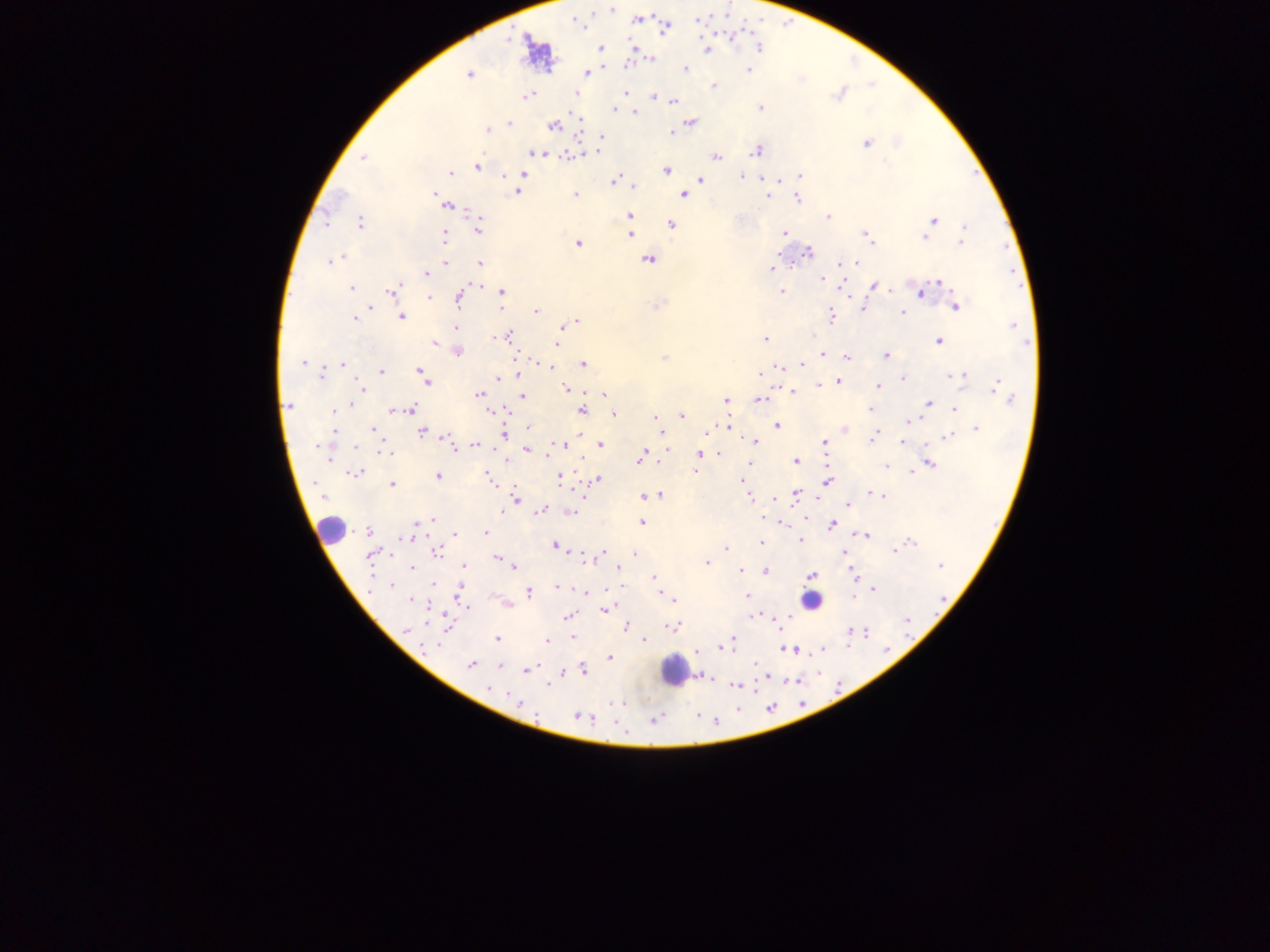

Approximate centers as {x, y} in pixels.
Summary:
  - Leukocyte locations: {330, 529}, {810, 601}, {674, 670}
  - Plasmodium parasite locations: {612, 8}, {697, 19}, {576, 20}, {637, 20}, {665, 29}, {530, 45}, {759, 47}, {601, 48}, {706, 49}, {651, 59}, {686, 70}, {748, 70}, {587, 73}, {469, 74}, {714, 86}, {625, 92}, {575, 93}, {838, 94}, {527, 95}, {654, 96}, {673, 100}, {760, 108}, {614, 110}, {635, 112}, {690, 122}, {509, 123}, {553, 126}, {487, 130}, {670, 132}, {602, 137}, {866, 144}, {598, 149}, {757, 150}, {535, 153}, {567, 156}, {715, 156}, {363, 158}, {477, 167}, {666, 171}, {451, 173}, {523, 174}, {800, 175}, {741, 176}, {701, 180}, {614, 181}, {635, 186}, {517, 191}, {434, 193}, {574, 194}, {683, 196}, {767, 196}, {798, 198}, {448, 207}, {630, 215}, {828, 216}, {934, 220}, {326, 221}, {360, 223}, {672, 225}, {964, 226}, {479, 227}, {784, 233}, {631, 234}, {444, 235}, {867, 237}, {925, 237}, {870, 240}, {962, 240}, {577, 244}, {808, 252}, {340, 259}, {649, 259}, {331, 261}, {445, 262}, {479, 262}, {854, 263}, {772, 269}, {425, 274}, {822, 279}, {941, 282}, {478, 285}, {875, 286}, {351, 288}, {391, 291}, {781, 291}, {501, 292}, {922, 292}, {429, 298}, {459, 299}, {658, 306}, {956, 306}, {863, 307}, {369, 308}, {535, 311}, {903, 312}, {402, 316}, {831, 316}, {355, 317}, {576, 322}, {568, 324}, {1013, 326}, {456, 328}, {561, 328}, {498, 337}, {507, 337}, {764, 339}, {938, 342}, {434, 343}, {557, 344}, {458, 352}, {822, 354}, {885, 355}, {665, 358}, {847, 358}, {302, 363}, {343, 364}, {583, 364}, {802, 365}, {549, 366}, {780, 366}, {420, 370}, {321, 371}, {381, 372}, {519, 373}, {761, 373}, {960, 376}, {498, 379}, {903, 379}, {425, 380}, {838, 382}, {819, 384}, {878, 386}, {997, 386}, {363, 388}, {565, 388}, {793, 391}, {478, 394}, {604, 394}, {523, 397}, {760, 399}, {1010, 399}, {726, 400}, {929, 404}, {290, 405}, {350, 405}, {410, 408}, {869, 409}, {955, 409}, {335, 410}, {393, 410}, {490, 411}, {582, 411}, {614, 414}, {682, 415}, {657, 418}, {911, 420}, {726, 425}, {777, 426}, {529, 427}, {374, 429}, {845, 429}, {976, 429}, {334, 431}, {422, 433}, {504, 435}, {663, 436}, {873, 437}, {947, 437}, {754, 441}, {824, 442}, {903, 442}, {601, 444}, {451, 445}, {476, 445}, {562, 445}, {355, 446}, {321, 448}, {528, 449}, {667, 450}, {386, 452}, {719, 454}, {699, 455}, {642, 457}, {327, 458}, {795, 461}, {930, 464}, {887, 466}, {912, 472}, {355, 473}, {438, 477}, {489, 477}, {560, 479}, {597, 480}, {743, 481}, {827, 482}, {392, 484}, {796, 493}, {875, 494}, {660, 495}, {644, 496}, {879, 496}, {322, 497}, {749, 498}, {515, 499}, {848, 505}, {543, 509}, {503, 512}, {572, 513}, {430, 521}, {421, 522}, {642, 523}, {832, 525}, {368, 532}, {485, 533}, {454, 534}, {865, 536}, {406, 538}, {800, 540}, {761, 542}, {911, 542}, {554, 545}, {725, 548}, {894, 551}, {437, 552}, {603, 552}, {844, 553}, {370, 554}, {634, 554}, {497, 558}, {707, 562}, {463, 566}, {941, 566}, {513, 567}, {412, 568}, {618, 568}, {741, 570}, {766, 571}, {812, 575}, {654, 577}, {855, 577}, {433, 584}, {391, 586}, {559, 587}, {874, 589}, {586, 591}, {529, 592}, {459, 594}, {747, 596}, {668, 597}, {411, 601}, {466, 606}, {604, 611}, {568, 616}, {755, 616}, {908, 620}, {626, 627}, {674, 627}, {405, 630}, {865, 633}, {851, 634}, {573, 637}, {496, 638}, {644, 640}, {732, 640}, {546, 641}, {730, 644}, {436, 646}, {725, 646}, {793, 650}, {697, 652}, {610, 658}, {471, 665}, {500, 665}, {756, 666}, {583, 669}, {529, 670}, {560, 673}, {707, 677}, {549, 685}, {736, 685}, {489, 688}, {520, 703}, {579, 716}, {655, 720}
  - Preparation: thick blood film
  - Field of view: single
  - Image size: 1270×952 pixels
  - Country: Ghana
  - Capture: mobile-phone photograph through a microscope